Classify this cell by malaria status.
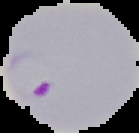

It is parasitized.

preparation: thin blood smear
image_size: 139×133 pixels
image_type: segmented cell region on a black background